Outline each blood parasite and name the species.
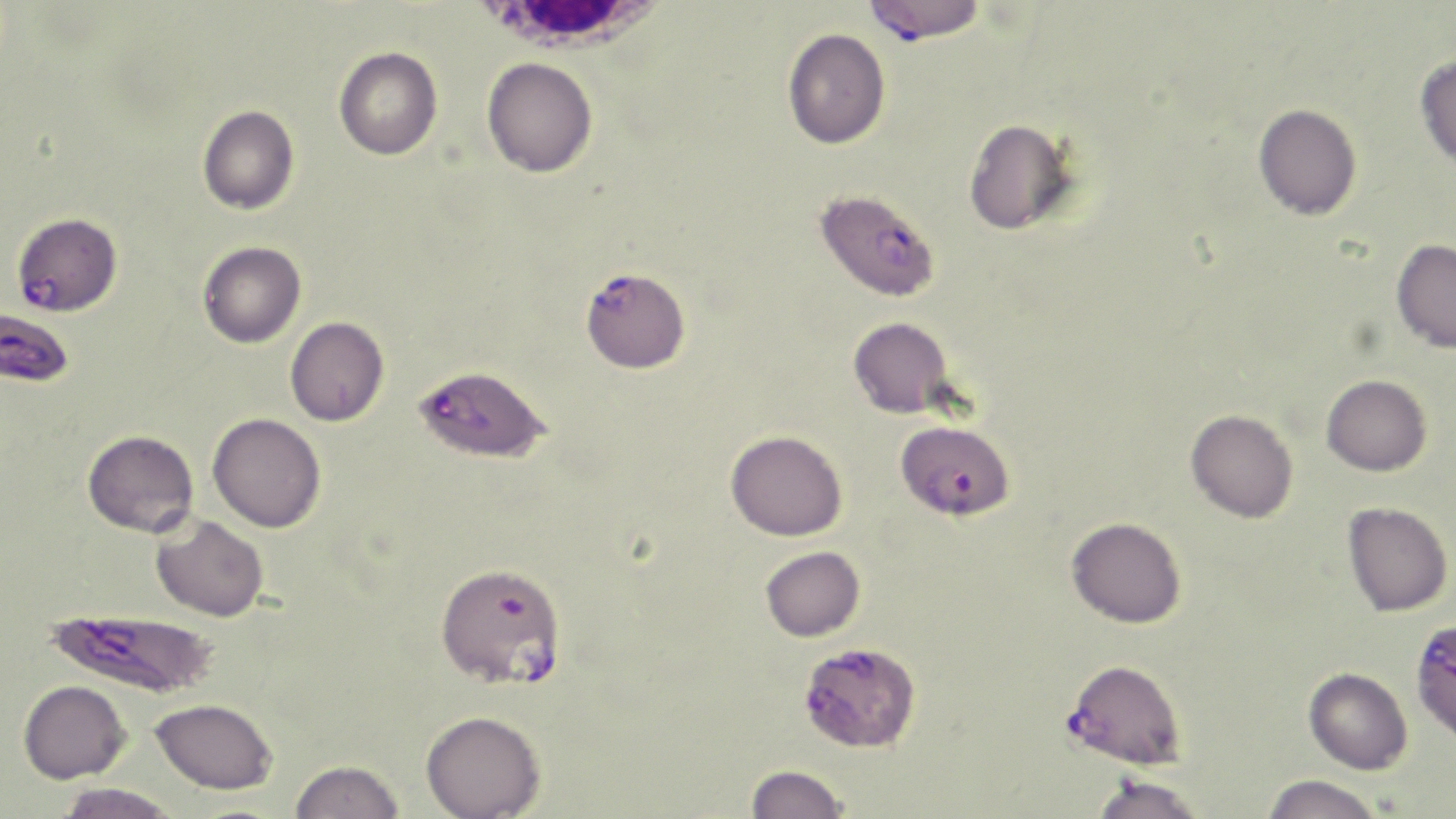
Approximate bounding boxes as [x1, y1, x2, y2] in pixels.
Plasmodium falciparum-infected red blood cells: [863, 0, 987, 42], [814, 188, 941, 302], [10, 211, 123, 316], [581, 267, 690, 373], [0, 306, 75, 387], [416, 365, 554, 466], [898, 428, 1018, 525], [435, 560, 568, 690], [45, 606, 219, 699], [1413, 617, 1456, 744], [802, 647, 920, 758], [1064, 658, 1187, 768].
No Plasmodium ovale, Plasmodium malariae, Plasmodium vivax, Babesia divergens, or Trypanosoma brucei observed.

slide_level_diagnosis: Plasmodium falciparum
preparation: thin blood film
modality: optical microscopy
image_size: 1456×819 pixels
stain: May-Grünwald-Giemsa
magnification: 1000x
white_blood_cell_locations: 'approximate bounding boxes as [x1, y1, x2, y2] in pixels: [471, 0, 669, 62]'
field_of_view: single
uninfected_red_blood_cell_locations: 'approximate bounding boxes as [x1, y1, x2, y2] in pixels: [782, 28, 890, 149], [333, 46, 443, 160], [1415, 54, 1456, 168], [482, 57, 597, 178], [1253, 103, 1362, 221], [197, 105, 300, 215], [963, 118, 1079, 235], [1391, 239, 1456, 353], [198, 241, 306, 348], [285, 316, 389, 426], [848, 316, 954, 418], [1321, 374, 1432, 476], [1186, 409, 1298, 522], [207, 412, 326, 532], [82, 429, 199, 538], [726, 430, 848, 541], [1343, 502, 1452, 616], [152, 515, 269, 622], [1066, 517, 1187, 628], [760, 546, 865, 642], [1304, 667, 1413, 774], [18, 680, 131, 783], [150, 697, 278, 794], [420, 710, 546, 819], [290, 759, 404, 819], [745, 764, 850, 819], [1261, 774, 1385, 819], [1089, 775, 1208, 819], [55, 783, 182, 818]'